Name the blood parasite species.
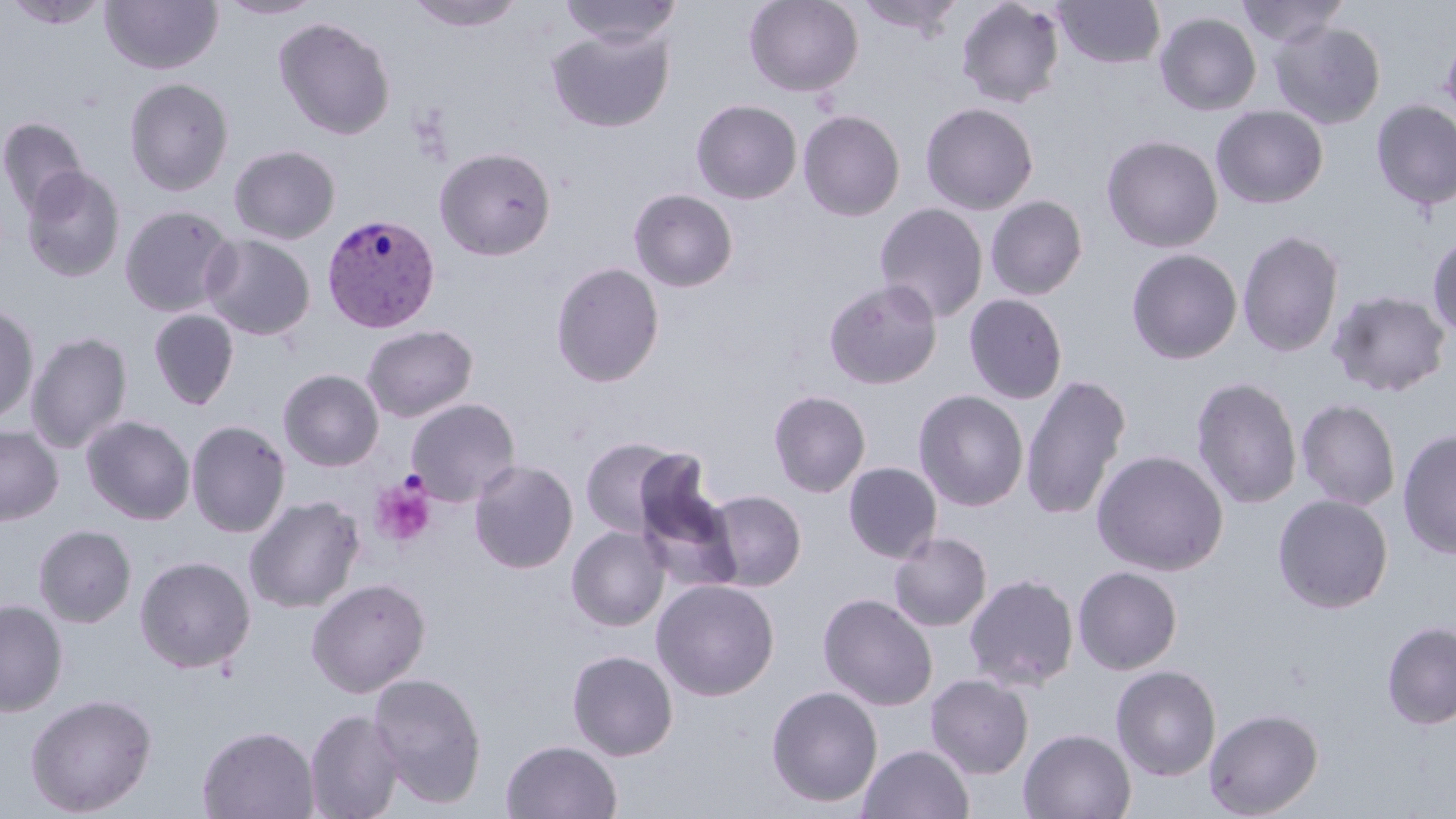
Plasmodium vivax.

Approximate bounding boxes as [x1, y1, x2, y2] in pixels. Plasmodium vivax-infected red blood cell locations: [321, 213, 441, 333]. Platelet locations: [370, 477, 436, 547]. Uninfected red blood cell locations: [6, 0, 110, 28], [217, 0, 325, 19], [406, 0, 527, 31], [557, 0, 684, 47], [744, 0, 864, 98], [853, 0, 966, 38], [956, 0, 1065, 108], [1053, 0, 1165, 69], [1235, 0, 1349, 47], [101, 1, 223, 74], [1154, 12, 1262, 116], [273, 17, 396, 140], [1269, 21, 1386, 130], [547, 25, 674, 132], [1441, 37, 1456, 124], [124, 77, 234, 196], [691, 99, 802, 204], [1371, 99, 1456, 211], [920, 102, 1039, 215], [1211, 105, 1328, 209], [798, 110, 905, 221], [0, 117, 90, 219], [1101, 134, 1223, 253], [229, 145, 340, 244], [219, 146, 328, 341], [434, 146, 556, 260], [21, 166, 126, 283], [628, 188, 738, 292], [985, 195, 1088, 300], [874, 203, 988, 323], [119, 205, 236, 318], [1237, 228, 1344, 359], [1427, 232, 1456, 340], [201, 233, 315, 341], [1126, 248, 1243, 364], [551, 261, 664, 387], [823, 279, 943, 390], [1326, 289, 1452, 398], [964, 294, 1068, 405], [0, 302, 39, 426], [148, 309, 240, 411], [361, 324, 478, 422], [26, 331, 132, 454], [278, 369, 384, 471], [1020, 373, 1131, 521], [1191, 376, 1303, 509], [768, 389, 871, 497], [913, 389, 1029, 511], [406, 398, 521, 506], [1296, 398, 1401, 511], [82, 415, 195, 525], [186, 420, 291, 537], [0, 426, 63, 526], [1397, 429, 1456, 561], [579, 436, 689, 535], [1092, 449, 1229, 576], [469, 460, 578, 574], [843, 462, 942, 563], [703, 489, 806, 591], [1273, 494, 1393, 613], [244, 495, 365, 613], [33, 524, 136, 627], [566, 526, 669, 631], [888, 532, 991, 632], [135, 555, 256, 673], [1072, 566, 1183, 674], [964, 573, 1080, 691], [307, 578, 431, 697], [651, 579, 780, 700], [818, 593, 938, 711], [0, 599, 68, 716], [1381, 621, 1456, 730], [566, 649, 678, 761], [1111, 664, 1222, 781], [368, 672, 487, 808], [925, 674, 1033, 779], [766, 685, 883, 808], [25, 693, 157, 816], [1204, 707, 1324, 818], [304, 708, 404, 819], [198, 725, 319, 819], [1019, 728, 1136, 819], [500, 740, 623, 819], [857, 744, 974, 819]. Single field of view. Thin blood film. May-Grünwald-Giemsa-stained preparation. 1000x magnification. Image is 1456×819 pixels. Optical microscopy.